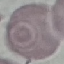
{
  "malaria_status": "uninfected",
  "capture": "smartphone camera at the microscope eyepiece",
  "preparation": "thin blood film",
  "image_type": "automatically extracted cell patch, resized to 64 × 64 pixels",
  "stain": "Giemsa"
}